State which parasite is depicted.
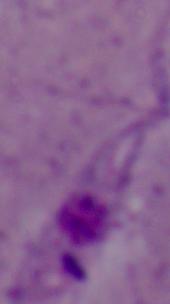
Leishmania.

modality = photomicrograph
magnification = 1000x